Comment on the morphology of the red blood cells.
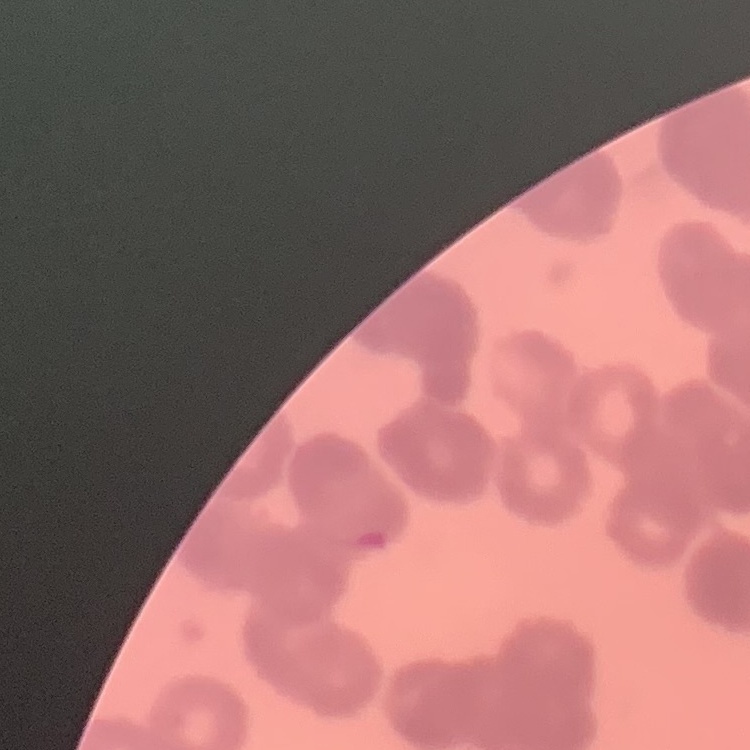

They show rouleaux formation.

Thin blood film. One tile cut from a larger photomicrograph. Field's or Giemsa stain.